State the blood parasite species.
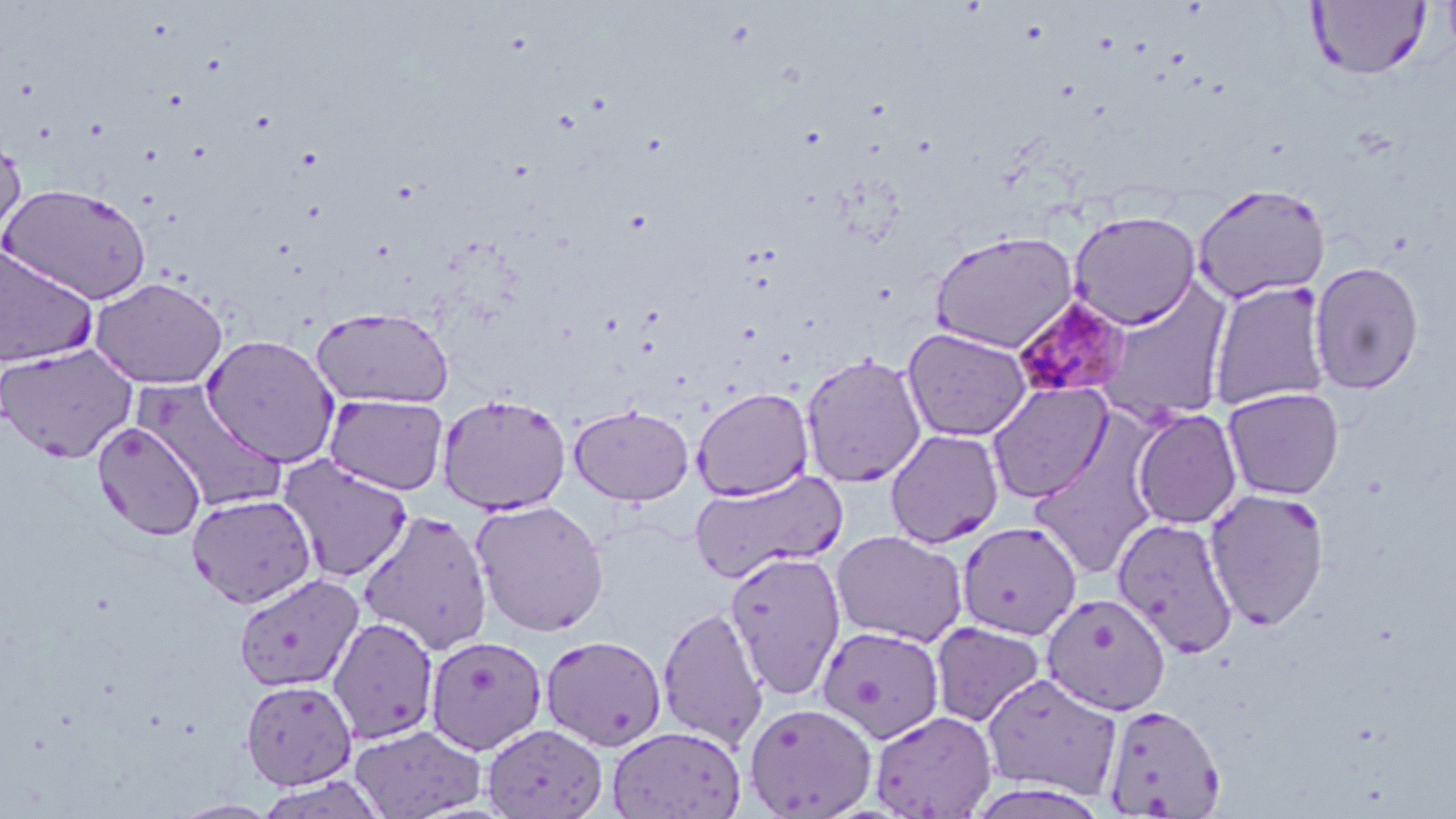
Plasmodium malariae.

Approximate bounding boxes as (x1,y1)-(x2,y2) corner pairs in pixels. Plasmodium malariae-infected red blood cell locations: (1013,297)-(1132,404). Uninfected red blood cell locations: (1308,1)-(1430,80), (0,125)-(26,245), (1,183)-(152,305), (1191,183)-(1332,304), (1067,210)-(1201,329), (929,230)-(1080,353), (0,243)-(98,369), (1309,261)-(1425,394), (90,277)-(228,389), (1093,280)-(1235,426), (1207,281)-(1332,411), (311,306)-(455,408), (902,327)-(1033,442), (201,333)-(341,468), (0,344)-(137,463), (800,353)-(927,488), (131,378)-(288,513), (986,381)-(1113,503), (1222,386)-(1345,500), (691,387)-(814,502), (324,393)-(449,495), (436,393)-(572,514), (569,404)-(694,506), (1130,408)-(1243,529), (93,421)-(206,541), (884,429)-(1004,548), (1028,453)-(1155,580), (278,455)-(414,583), (689,469)-(848,585), (1204,486)-(1331,631), (186,493)-(317,608), (470,499)-(610,636), (357,509)-(493,653), (1112,516)-(1239,658), (957,520)-(1082,639), (831,529)-(968,647), (726,550)-(846,700), (233,574)-(364,692), (1041,592)-(1172,715), (657,606)-(768,750), (327,616)-(440,745), (929,620)-(1047,728), (817,625)-(945,744), (540,634)-(667,752), (424,635)-(548,755), (981,672)-(1123,799), (241,679)-(358,790), (743,702)-(877,818), (1100,703)-(1226,817), (870,710)-(997,818), (349,723)-(487,819), (482,723)-(608,818), (607,724)-(747,819). Light microscopy. May-Grünwald-Giemsa-stained preparation. Thin blood smear. One field of a larger specimen. Image is 1456×819 pixels. 1000x magnification.